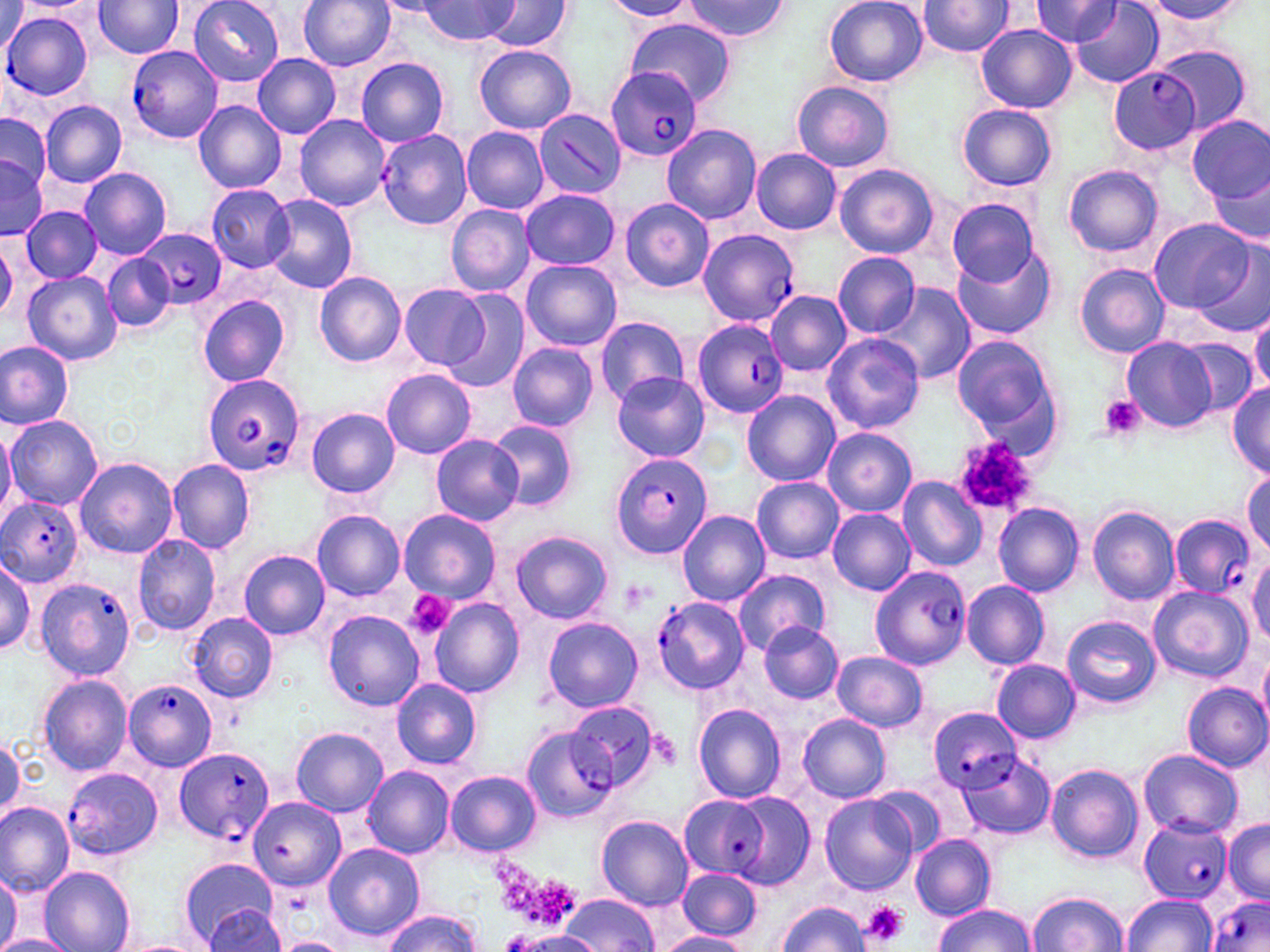
Summary:
  - Coordinate format: approximate bounding boxes as named x1/y1/x2/y2 corners in pixels
  - Platelet locations: (x1=1099, y1=395, x2=1145, y2=441), (x1=954, y1=439, x2=1035, y2=517), (x1=403, y1=590, x2=453, y2=639), (x1=520, y1=876, x2=583, y2=932), (x1=861, y1=901, x2=911, y2=947)
  - Plasmodium falciparum-infected red blood cell locations: (x1=2, y1=12, x2=93, y2=103), (x1=127, y1=47, x2=224, y2=145), (x1=606, y1=64, x2=703, y2=164), (x1=1109, y1=67, x2=1199, y2=153), (x1=376, y1=128, x2=472, y2=231), (x1=136, y1=226, x2=226, y2=310), (x1=697, y1=228, x2=799, y2=327), (x1=691, y1=318, x2=788, y2=416), (x1=202, y1=375, x2=309, y2=475), (x1=610, y1=450, x2=714, y2=559), (x1=0, y1=496, x2=83, y2=588), (x1=1171, y1=513, x2=1257, y2=600), (x1=870, y1=564, x2=972, y2=668), (x1=37, y1=576, x2=134, y2=681), (x1=123, y1=679, x2=219, y2=772), (x1=928, y1=707, x2=1020, y2=790), (x1=173, y1=745, x2=276, y2=845), (x1=65, y1=767, x2=165, y2=861), (x1=678, y1=796, x2=767, y2=879), (x1=1140, y1=819, x2=1232, y2=904), (x1=1207, y1=896, x2=1270, y2=952)
  - Uninfected red blood cell locations: (x1=189, y1=0, x2=284, y2=86), (x1=299, y1=0, x2=396, y2=71), (x1=825, y1=0, x2=927, y2=87), (x1=1030, y1=0, x2=1122, y2=46), (x1=15, y1=1, x2=99, y2=15), (x1=420, y1=1, x2=517, y2=45), (x1=482, y1=1, x2=573, y2=54), (x1=600, y1=1, x2=697, y2=22), (x1=684, y1=1, x2=788, y2=43), (x1=1144, y1=1, x2=1247, y2=26), (x1=93, y1=2, x2=184, y2=59), (x1=917, y1=2, x2=1015, y2=58), (x1=1070, y1=2, x2=1164, y2=89), (x1=626, y1=20, x2=736, y2=106), (x1=976, y1=25, x2=1077, y2=113), (x1=1152, y1=42, x2=1255, y2=135), (x1=475, y1=45, x2=576, y2=134), (x1=253, y1=54, x2=341, y2=138), (x1=356, y1=58, x2=449, y2=146), (x1=791, y1=80, x2=895, y2=173), (x1=41, y1=100, x2=126, y2=188), (x1=193, y1=100, x2=286, y2=194), (x1=959, y1=104, x2=1057, y2=191), (x1=0, y1=111, x2=52, y2=202), (x1=293, y1=114, x2=390, y2=211), (x1=1187, y1=116, x2=1269, y2=202), (x1=661, y1=124, x2=761, y2=224), (x1=462, y1=126, x2=548, y2=213), (x1=752, y1=148, x2=842, y2=234), (x1=0, y1=150, x2=47, y2=239), (x1=834, y1=163, x2=938, y2=259), (x1=1064, y1=164, x2=1163, y2=258), (x1=78, y1=167, x2=171, y2=259), (x1=1207, y1=167, x2=1270, y2=246), (x1=206, y1=184, x2=296, y2=271), (x1=521, y1=188, x2=621, y2=270), (x1=262, y1=193, x2=357, y2=294), (x1=620, y1=198, x2=714, y2=293), (x1=946, y1=198, x2=1038, y2=287), (x1=445, y1=204, x2=536, y2=296), (x1=21, y1=205, x2=103, y2=283), (x1=1149, y1=218, x2=1255, y2=313), (x1=1196, y1=243, x2=1270, y2=338), (x1=953, y1=244, x2=1057, y2=342), (x1=833, y1=252, x2=920, y2=336), (x1=103, y1=253, x2=175, y2=332), (x1=522, y1=259, x2=622, y2=352), (x1=1075, y1=262, x2=1171, y2=357), (x1=22, y1=271, x2=122, y2=365), (x1=315, y1=272, x2=405, y2=367), (x1=879, y1=284, x2=975, y2=383), (x1=398, y1=285, x2=490, y2=369), (x1=441, y1=289, x2=532, y2=394), (x1=766, y1=291, x2=850, y2=376), (x1=197, y1=294, x2=291, y2=386), (x1=1249, y1=313, x2=1270, y2=396), (x1=593, y1=315, x2=691, y2=406), (x1=822, y1=333, x2=924, y2=435), (x1=953, y1=335, x2=1061, y2=445), (x1=1122, y1=336, x2=1216, y2=432), (x1=1178, y1=339, x2=1258, y2=417), (x1=1, y1=342, x2=73, y2=430), (x1=506, y1=342, x2=598, y2=431), (x1=381, y1=369, x2=477, y2=459), (x1=612, y1=371, x2=710, y2=463), (x1=1227, y1=383, x2=1270, y2=479), (x1=742, y1=389, x2=839, y2=485), (x1=306, y1=407, x2=400, y2=498), (x1=5, y1=415, x2=102, y2=510), (x1=488, y1=419, x2=579, y2=512), (x1=0, y1=422, x2=15, y2=521), (x1=822, y1=428, x2=917, y2=516), (x1=429, y1=434, x2=523, y2=527), (x1=73, y1=457, x2=179, y2=559), (x1=168, y1=460, x2=255, y2=555), (x1=1244, y1=471, x2=1270, y2=555), (x1=752, y1=476, x2=844, y2=563), (x1=898, y1=476, x2=986, y2=573), (x1=994, y1=503, x2=1085, y2=595), (x1=1088, y1=506, x2=1180, y2=606), (x1=827, y1=508, x2=915, y2=595), (x1=398, y1=509, x2=500, y2=602), (x1=311, y1=510, x2=405, y2=601), (x1=677, y1=510, x2=770, y2=606), (x1=511, y1=531, x2=612, y2=625), (x1=132, y1=534, x2=222, y2=637), (x1=238, y1=551, x2=330, y2=640), (x1=1247, y1=557, x2=1269, y2=647), (x1=0, y1=558, x2=36, y2=655), (x1=733, y1=569, x2=831, y2=655), (x1=962, y1=580, x2=1051, y2=670), (x1=1147, y1=586, x2=1252, y2=682), (x1=399, y1=589, x2=465, y2=639), (x1=654, y1=596, x2=750, y2=694), (x1=429, y1=597, x2=524, y2=696), (x1=323, y1=609, x2=425, y2=711), (x1=187, y1=612, x2=278, y2=702), (x1=1061, y1=614, x2=1162, y2=708), (x1=543, y1=618, x2=643, y2=712), (x1=758, y1=622, x2=845, y2=704), (x1=831, y1=651, x2=928, y2=731), (x1=1259, y1=651, x2=1270, y2=730), (x1=992, y1=660, x2=1081, y2=743), (x1=38, y1=676, x2=132, y2=775), (x1=391, y1=678, x2=482, y2=769), (x1=1182, y1=682, x2=1270, y2=772), (x1=568, y1=698, x2=661, y2=793), (x1=693, y1=704, x2=787, y2=803), (x1=798, y1=714, x2=892, y2=802), (x1=293, y1=727, x2=387, y2=816), (x1=522, y1=728, x2=616, y2=819), (x1=0, y1=736, x2=24, y2=823), (x1=1137, y1=749, x2=1243, y2=838), (x1=956, y1=753, x2=1056, y2=841), (x1=1045, y1=763, x2=1144, y2=864), (x1=361, y1=765, x2=455, y2=860), (x1=446, y1=770, x2=540, y2=856), (x1=870, y1=785, x2=945, y2=859), (x1=729, y1=792, x2=814, y2=888), (x1=820, y1=794, x2=919, y2=894), (x1=248, y1=797, x2=344, y2=891), (x1=0, y1=801, x2=76, y2=895), (x1=596, y1=815, x2=693, y2=910), (x1=1222, y1=820, x2=1270, y2=903), (x1=911, y1=833, x2=995, y2=920), (x1=323, y1=842, x2=424, y2=941), (x1=180, y1=859, x2=278, y2=947), (x1=40, y1=867, x2=135, y2=951), (x1=677, y1=868, x2=761, y2=940), (x1=0, y1=870, x2=21, y2=952), (x1=566, y1=892, x2=655, y2=952), (x1=1028, y1=892, x2=1128, y2=951), (x1=1122, y1=894, x2=1216, y2=951), (x1=778, y1=900, x2=869, y2=951), (x1=934, y1=903, x2=1034, y2=952), (x1=202, y1=904, x2=286, y2=952), (x1=384, y1=911, x2=482, y2=951), (x1=506, y1=932, x2=602, y2=952), (x1=657, y1=932, x2=751, y2=952), (x1=0, y1=934, x2=74, y2=952), (x1=276, y1=936, x2=348, y2=952), (x1=115, y1=938, x2=211, y2=952)
  - Slide-level diagnosis: Plasmodium falciparum
  - Field of view: single
  - Stain: May-Grünwald-Giemsa
  - Image size: 1270×952 pixels
  - Preparation: thin blood film
  - Modality: light microscopy
  - Magnification: 1000x